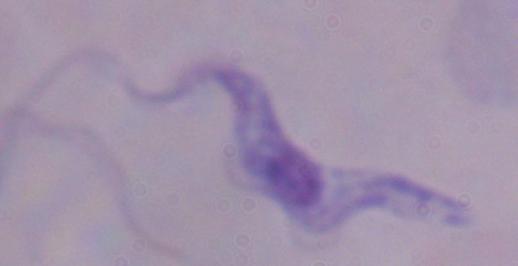

Summary:
  - Modality: photomicrograph
  - Identification: trypanosome
  - Magnification: 1000x